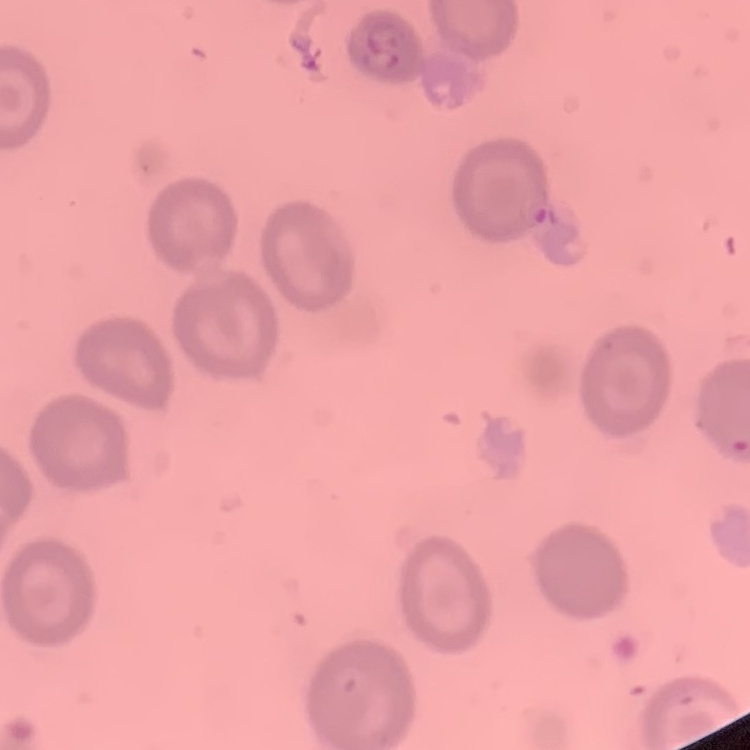
{
  "red_blood_cell_morphology": "no rouleaux formation",
  "preparation": "thin peripheral smear",
  "stain": "Field's or Giemsa",
  "image_type": "square crop of a larger photomicrograph"
}